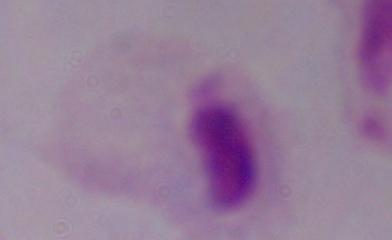 A trichomonad is seen. Micrograph. Captured at 1000x magnification.